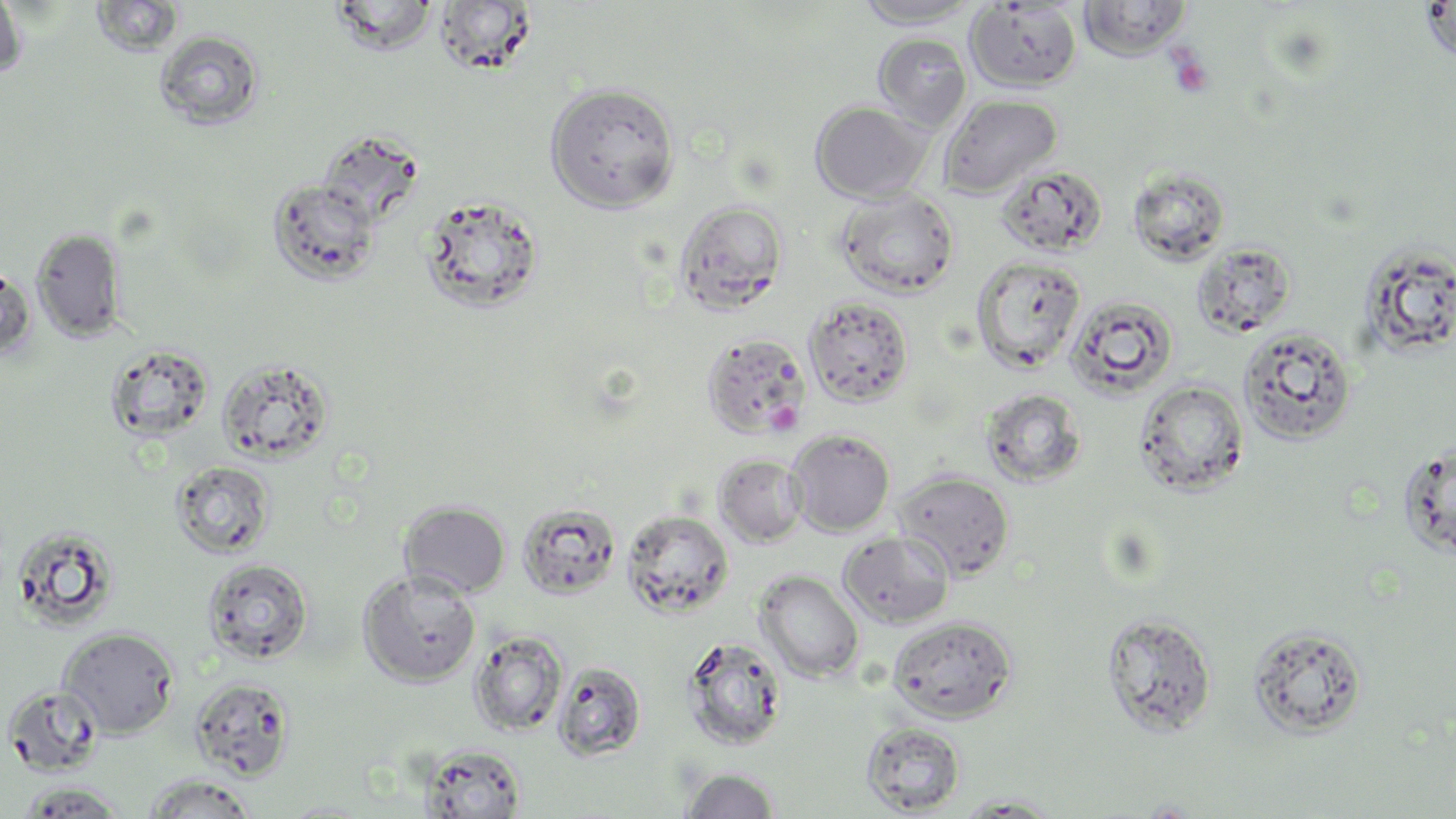
Summary:
  - Coordinate format: approximate bounding boxes as [x1, y1, x2, y2] in pixels
  - Platelet locations: [1168, 51, 1214, 98]
  - Uninfected red blood cell locations: [0, 0, 28, 80], [90, 0, 184, 58], [327, 0, 440, 55], [853, 0, 982, 28], [1078, 0, 1192, 59], [1418, 1, 1455, 63], [434, 2, 539, 77], [965, 2, 1082, 92], [154, 29, 265, 130], [873, 33, 972, 131], [545, 81, 681, 213], [938, 93, 1063, 198], [810, 101, 933, 203], [316, 129, 425, 226], [996, 165, 1107, 256], [267, 178, 380, 286], [834, 188, 959, 299], [418, 193, 546, 314], [673, 200, 789, 316], [32, 227, 127, 342], [1192, 241, 1298, 338], [1358, 242, 1456, 357], [970, 256, 1086, 373], [0, 263, 35, 361], [1064, 293, 1179, 400], [804, 296, 915, 407], [1238, 326, 1357, 446], [700, 332, 812, 440], [105, 343, 214, 444], [216, 357, 335, 465], [1134, 379, 1249, 497], [980, 387, 1087, 488], [786, 429, 895, 536], [1397, 443, 1456, 560], [713, 453, 809, 547], [170, 461, 275, 560], [891, 470, 1016, 579], [399, 501, 511, 597], [517, 501, 622, 600], [622, 509, 734, 619], [11, 526, 121, 633], [838, 531, 954, 627], [203, 557, 313, 665], [358, 570, 481, 686], [754, 570, 864, 682], [1100, 610, 1217, 737], [887, 615, 1017, 724], [1247, 623, 1368, 739], [58, 627, 179, 738], [468, 631, 568, 737], [681, 634, 789, 751], [553, 660, 647, 761], [189, 678, 295, 781], [3, 684, 103, 777], [860, 721, 966, 815], [420, 743, 527, 818], [679, 768, 781, 817], [140, 774, 260, 818], [14, 782, 130, 817], [950, 793, 1069, 816], [278, 800, 377, 817]
  - Slide-level diagnosis: no evidence of blood parasites
  - Magnification: 1000x
  - Preparation: thin blood film
  - Stain: May-Grünwald-Giemsa
  - Field of view: single
  - Modality: light microscopy
  - Image size: 1456×819 pixels